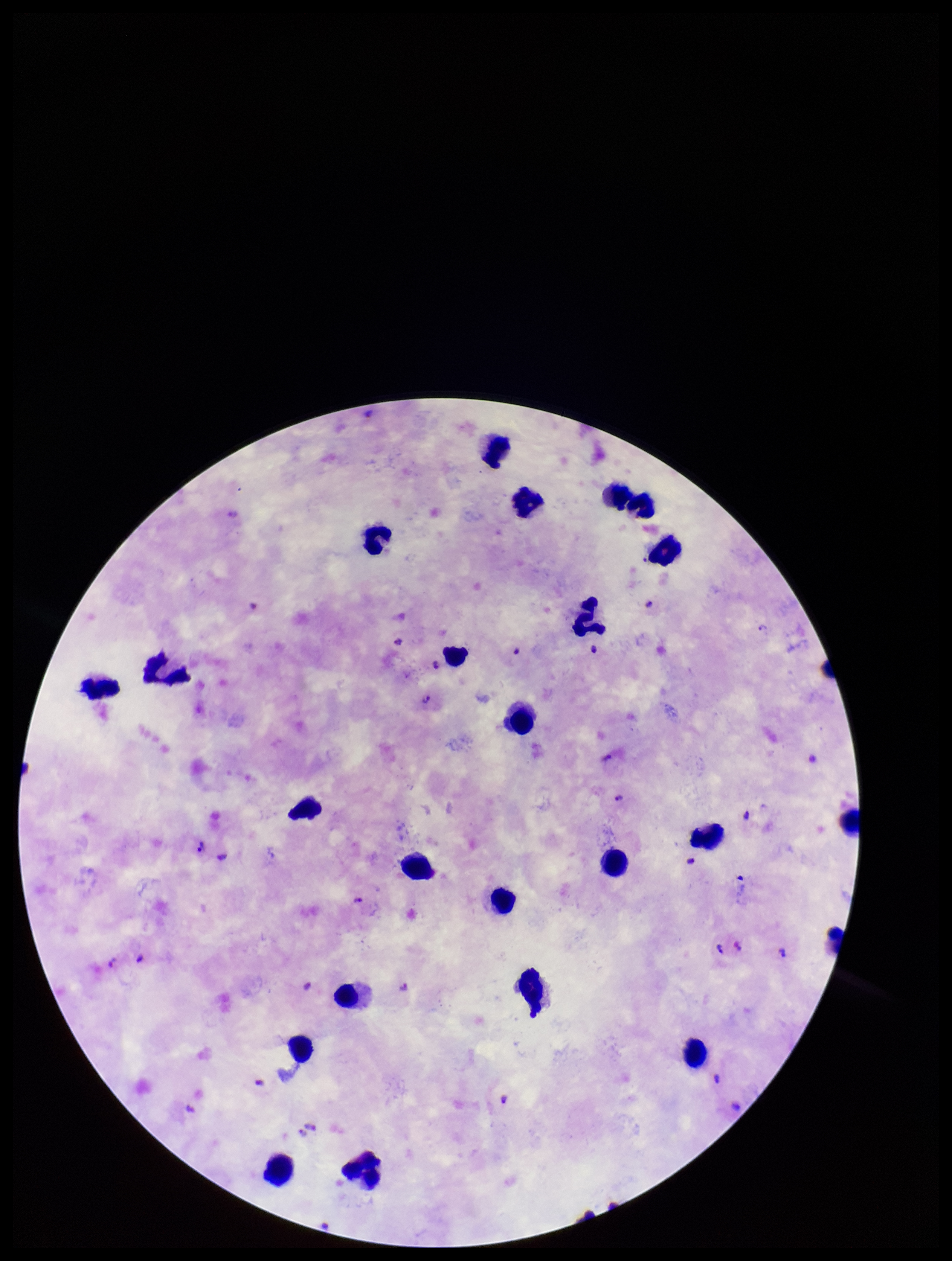
species_reported_for_this_patient: Plasmodium falciparum
field_of_view: single
leukocyte_count: 24
stain: Giemsa
preparation: thick blood smear
plasmodium_parasites: identified
capture: smartphone photograph through the microscope eyepiece
patient_malaria_status: infected
parasite_count: 14
image_size: 952×1261 pixels